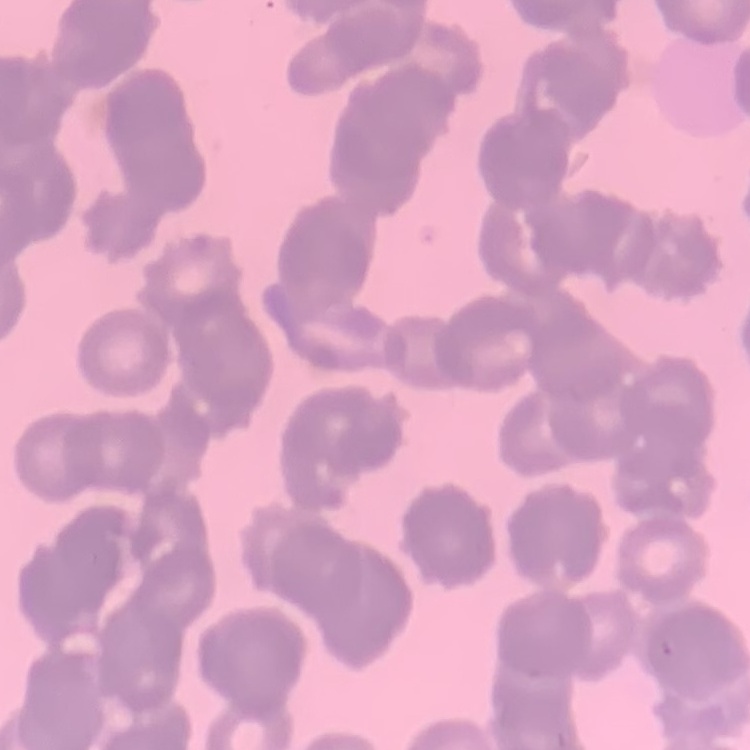

The red blood cells show rouleaux formation. One tile cut from a larger photomicrograph. Field's or Giemsa stain. Thin blood smear.